Identify the preparation type.
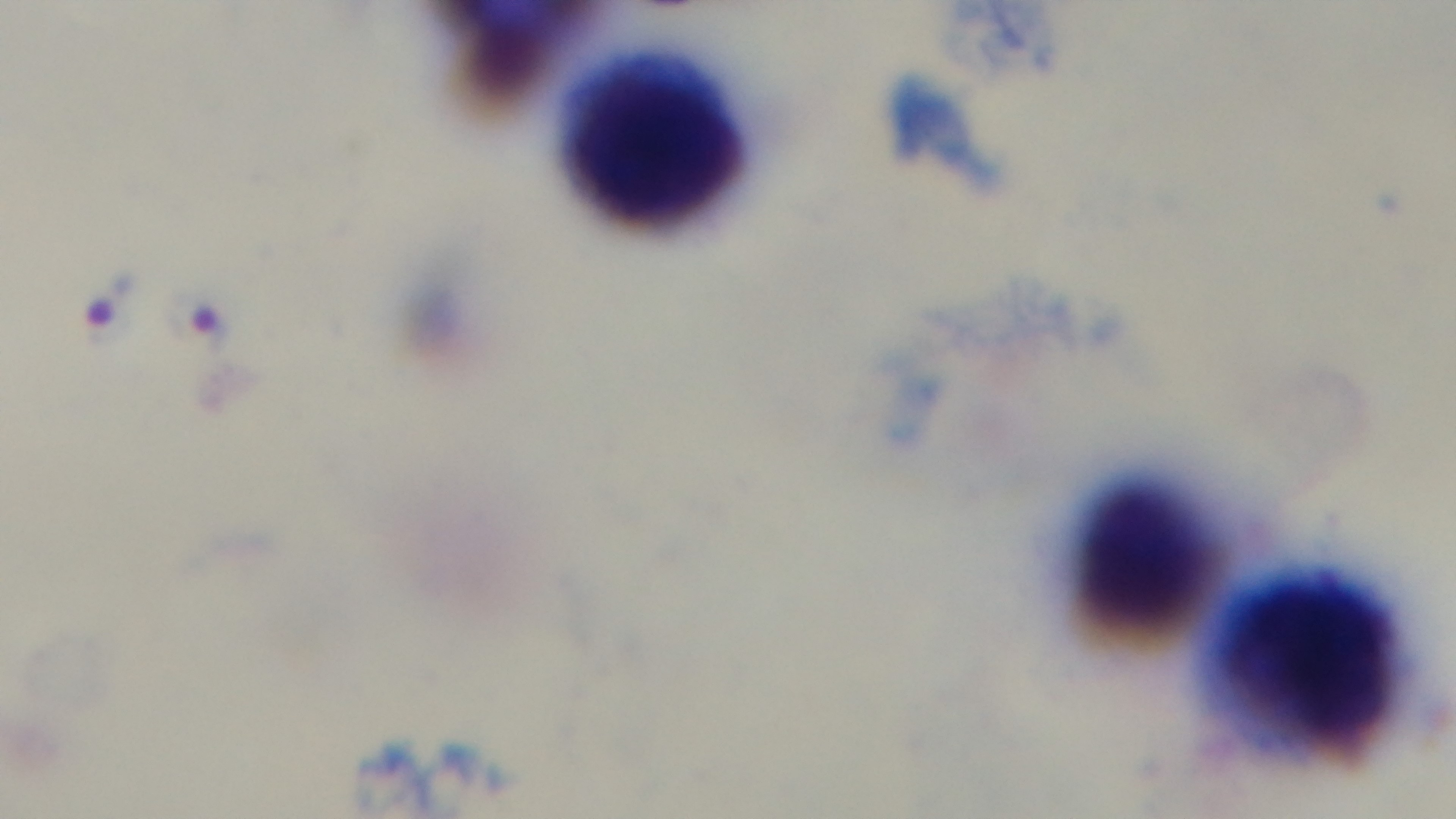

Thick.

objective = 100x oil immersion
modality = light microscopy
capture = mounted 4K digital camera
stain = Giemsa
field of view = single
malaria status = infected